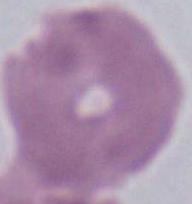
Summary:
  - Magnification: 1000x
  - Identification: red blood cell
  - Modality: photomicrograph